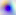

Toxoplasma gondii is shown. Captured at 400x magnification. Photomicrograph.